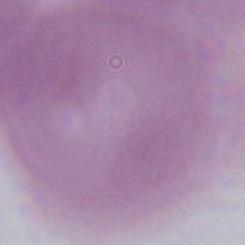
Summary:
  - Magnification: 1000x
  - Identification: red blood cell
  - Modality: photomicrograph